Outline each blood parasite and name the species.
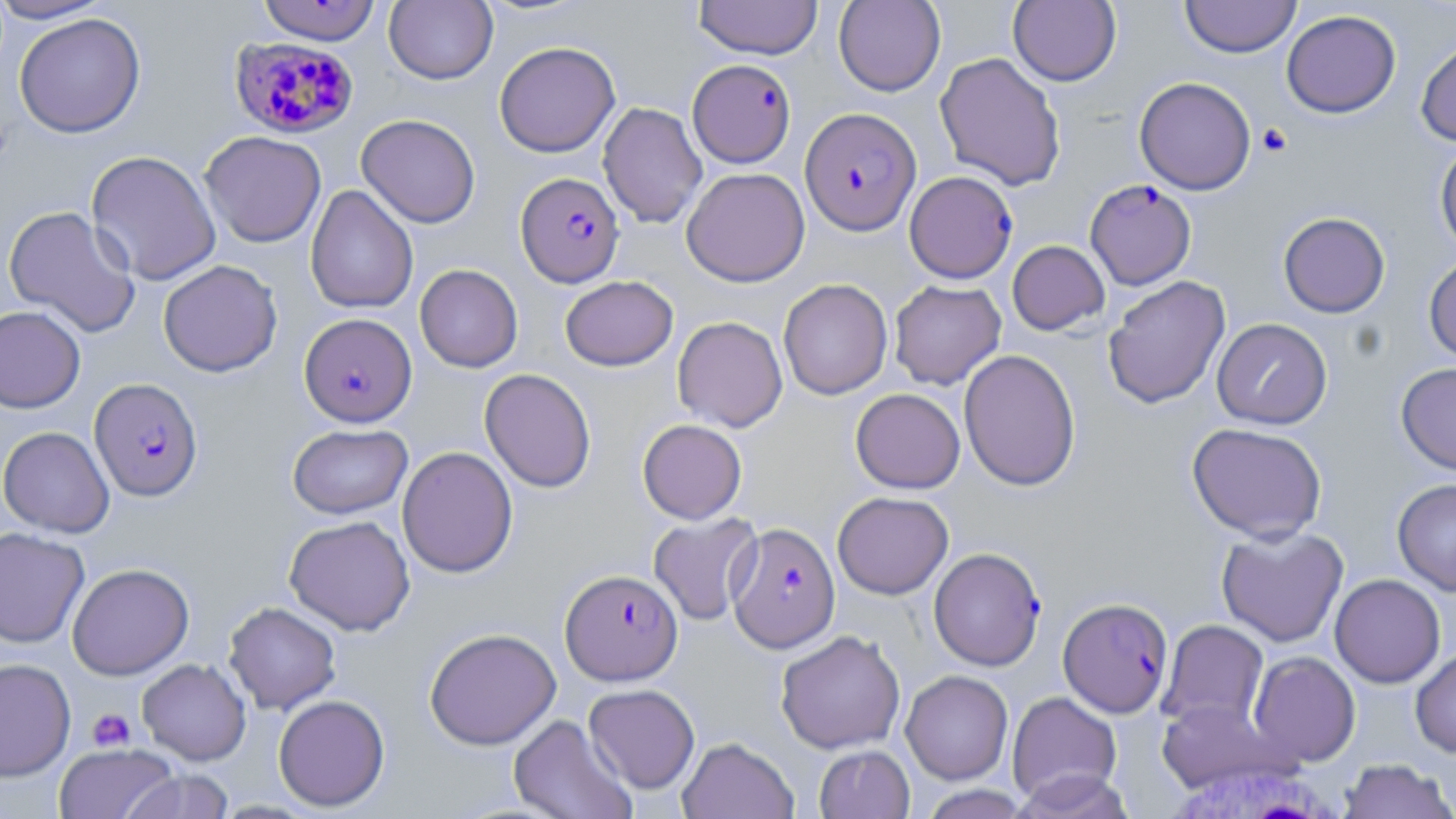
Approximate bounding boxes as [x1, y1, x2, y2] in pixels.
Plasmodium falciparum-infected red blood cells: [229, 37, 359, 139], [687, 59, 796, 168], [800, 107, 921, 235], [516, 172, 624, 287], [907, 172, 1020, 284], [1085, 179, 1196, 290], [299, 313, 417, 427], [89, 378, 202, 501], [727, 522, 840, 652], [929, 548, 1046, 671], [560, 568, 683, 686], [1059, 597, 1173, 717].
No Plasmodium ovale, Plasmodium malariae, Plasmodium vivax, Babesia divergens, or Trypanosoma brucei observed.

Summary:
  - Platelet locations: [1256, 123, 1292, 157], [88, 708, 136, 752]
  - Uninfected red blood cell locations: [0, 0, 114, 23], [693, 0, 824, 60], [833, 0, 946, 96], [1008, 0, 1121, 86], [1180, 0, 1301, 58], [257, 1, 382, 46], [384, 1, 498, 85], [1281, 9, 1401, 118], [14, 12, 146, 138], [1416, 34, 1456, 147], [494, 41, 620, 157], [934, 51, 1067, 191], [1134, 76, 1256, 195], [598, 101, 707, 228], [356, 114, 481, 228], [199, 130, 326, 248], [1434, 140, 1456, 254], [85, 150, 221, 286], [681, 167, 810, 286], [305, 185, 418, 314], [3, 205, 141, 337], [1278, 212, 1390, 318], [1007, 240, 1109, 335], [1423, 254, 1456, 362], [158, 259, 282, 377], [415, 264, 523, 373], [560, 275, 678, 371], [1103, 275, 1231, 409], [778, 278, 892, 400], [888, 280, 1007, 390], [0, 305, 85, 413], [672, 316, 788, 432], [1212, 318, 1332, 429], [959, 349, 1081, 491], [1396, 361, 1456, 474], [479, 368, 596, 493], [850, 388, 965, 493], [637, 419, 747, 524], [1187, 422, 1327, 543], [288, 423, 413, 518], [0, 426, 114, 537], [397, 446, 518, 578], [1392, 478, 1456, 596], [832, 491, 954, 599], [648, 513, 762, 626], [284, 515, 415, 636], [1216, 525, 1349, 647], [0, 527, 90, 648], [67, 563, 194, 680], [1330, 574, 1445, 688], [223, 601, 341, 715], [1157, 619, 1269, 732], [424, 627, 561, 750], [775, 630, 905, 754], [1410, 646, 1456, 757], [1248, 651, 1361, 766], [0, 658, 76, 781], [137, 658, 251, 765], [901, 670, 1013, 785], [583, 684, 700, 794], [1007, 691, 1122, 805], [273, 694, 390, 811], [1157, 699, 1283, 792], [507, 714, 637, 819], [677, 737, 798, 819], [54, 743, 179, 819], [814, 745, 914, 818], [1337, 759, 1455, 819], [1011, 769, 1134, 818], [121, 770, 235, 819], [918, 785, 1035, 818]
  - White blood cell locations: [1164, 761, 1350, 819]
  - Slide-level diagnosis: Plasmodium falciparum
  - Stain: May-Grünwald-Giemsa
  - Preparation: thin blood film
  - Magnification: 1000x
  - Image size: 1456×819 pixels
  - Field of view: one of a larger specimen
  - Modality: light microscopy